Locate every leukocyte (white blood cell).
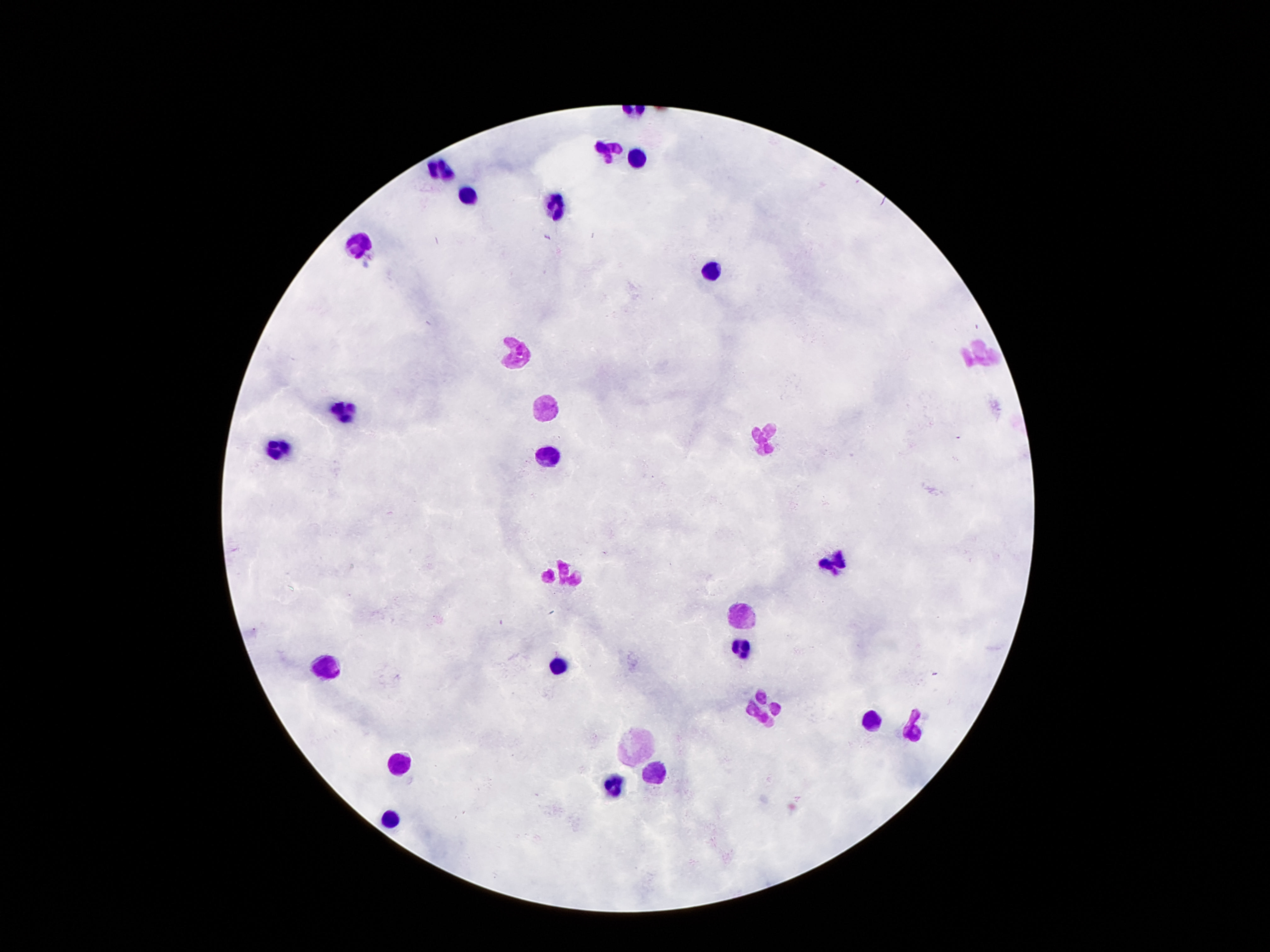

Approximate centers as [x, y] in pixels.
Leukocytes: [609, 149], [637, 158], [441, 169], [467, 197], [553, 209], [358, 248], [712, 272], [515, 353], [979, 353], [544, 403], [343, 412], [763, 443], [276, 450], [548, 458], [834, 564], [565, 573], [740, 619], [740, 647], [557, 665], [328, 670], [760, 705], [868, 717], [912, 734], [637, 745], [402, 760], [649, 777], [614, 787], [389, 820].

Summary:
  - Patient malaria status: uninfected
  - Image size: 1270×952 pixels
  - Magnification: 100x
  - Field of view: one from this slide
  - Preparation: thick blood smear
  - Capture: smartphone camera through the microscope eyepiece
  - Stain: Giemsa